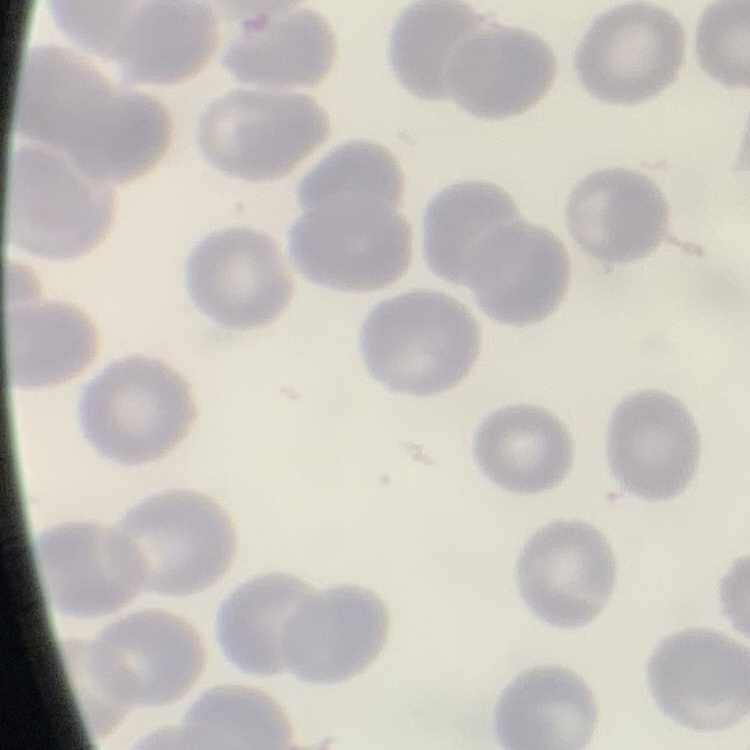
erythrocyte morphology = no rouleaux formation
preparation = thin blood film
stain = Field's or Giemsa
image type = one tile cut from a larger photomicrograph